Report the malaria status of this cell.
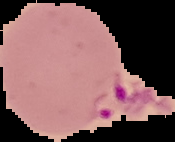

Parasitized.

Cell region segmented out of the field of view; the surrounding area is masked to black. Image is 175×142 pixels. From a thin blood smear.